Classify this cell by malaria status.
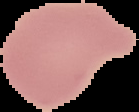

Uninfected.

image type = segmented cell region with the area outside set to black
preparation = thin blood film
image size = 139×112 pixels